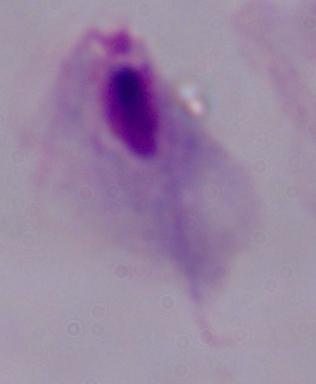
A trichomonad is shown. Micrograph. 1000x magnification.